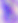
Toxoplasma gondii is seen. 400x magnification. Photomicrograph.